Describe the morphology of the erythrocytes.
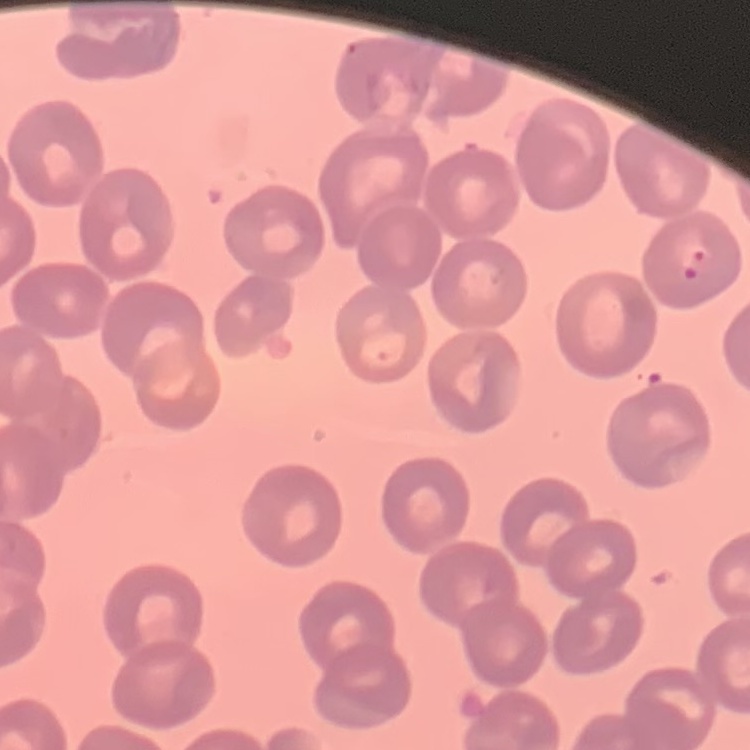
They show no rouleaux formation.

Square crop of a larger photomicrograph. Field's or Giemsa stain. Thin blood film.